Identify the blood parasite species.
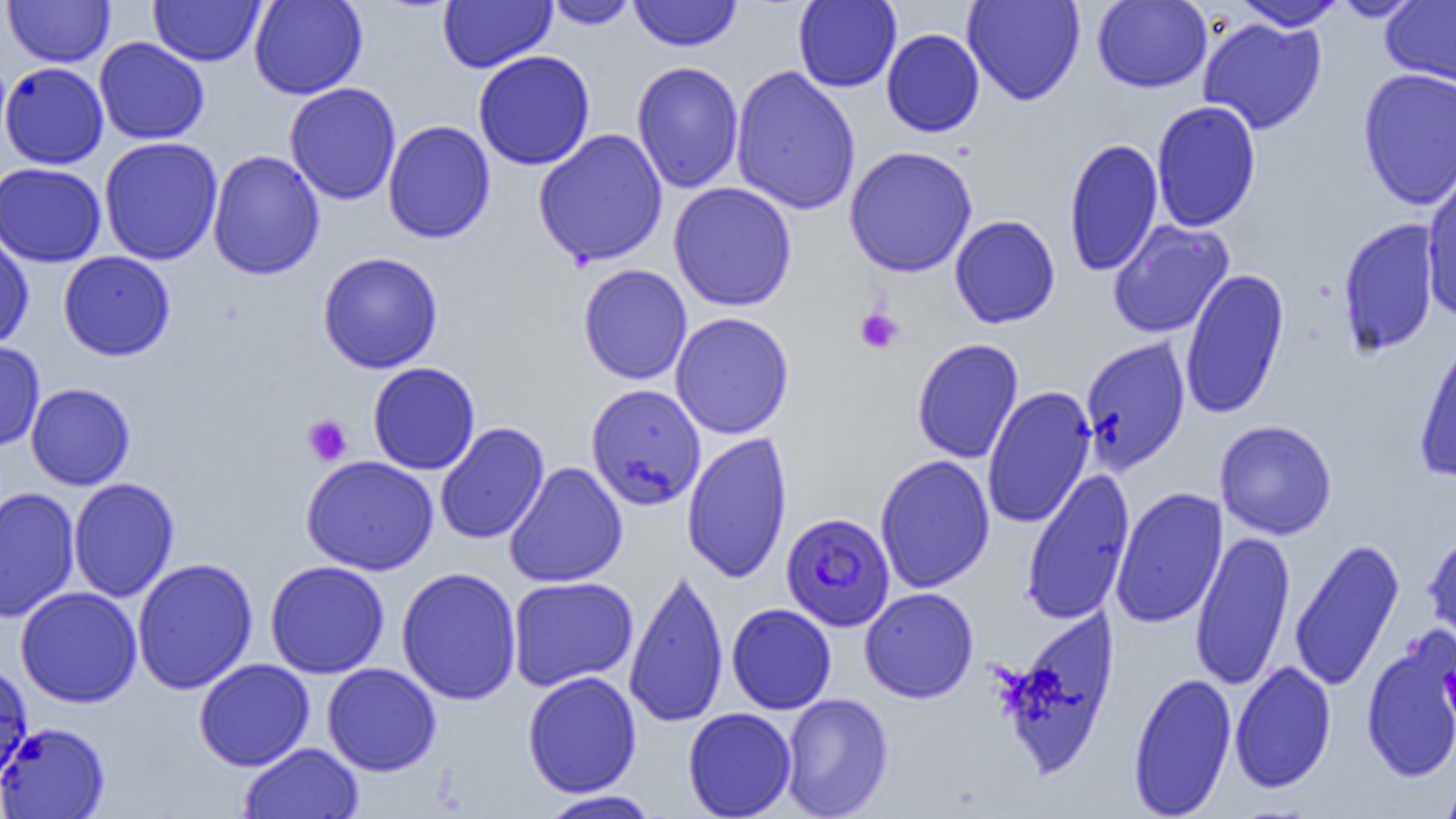

Plasmodium falciparum.

field of view = one of a larger specimen
preparation = thin blood film
image size = 1456×819 pixels
magnification = 1000x
modality = light microscopy
Plasmodium falciparum-infected red blood cell locations = approximate bounding boxes as (x1,y1)-(x2,y2) corner pairs in pixels: (781,512)-(895,631)
platelet locations = approximate bounding boxes as (x1,y1)-(x2,y2) corner pairs in pixels: (855,307)-(904,355), (302,414)-(353,466)
uninfected red blood cell locations = approximate bounding boxes as (x1,y1)-(x2,y2) corner pairs in pixels: (149,0)-(264,66), (249,0)-(367,99), (438,0)-(556,73), (544,0)-(639,29), (793,0)-(902,92), (962,0)-(1086,106), (1092,0)-(1212,93), (1331,0)-(1426,21), (3,1)-(115,67), (628,1)-(742,51), (1232,1)-(1347,31), (1381,1)-(1456,87), (1197,17)-(1327,135), (881,28)-(985,138), (94,37)-(210,144), (473,50)-(596,171), (631,61)-(744,193), (0,62)-(109,169), (731,65)-(861,216), (1357,68)-(1456,210), (284,83)-(401,205), (1151,100)-(1261,231), (383,120)-(496,244), (533,128)-(668,267), (99,136)-(223,265), (1064,137)-(1164,277), (844,146)-(978,277), (207,150)-(324,280), (0,162)-(106,266), (1421,166)-(1456,322), (668,182)-(797,311), (950,214)-(1061,329), (1337,218)-(1442,357), (1107,220)-(1234,338), (0,233)-(34,351), (58,251)-(175,361), (317,251)-(444,373), (578,263)-(692,384), (1179,268)-(1290,419), (670,312)-(794,439), (1413,329)-(1456,483), (1079,337)-(1190,474), (912,338)-(1024,464), (0,341)-(45,452), (367,362)-(480,474), (26,383)-(135,490), (586,384)-(706,511), (981,386)-(1096,529), (1215,420)-(1337,540), (434,422)-(550,544), (681,432)-(793,584), (875,454)-(994,594), (301,455)-(439,576), (504,461)-(628,588), (1020,468)-(1135,625), (67,477)-(180,602), (1111,486)-(1227,629), (0,487)-(80,621), (1190,530)-(1295,692), (1423,530)-(1456,652), (1289,537)-(1405,693), (132,557)-(258,694), (265,560)-(390,678), (624,565)-(729,729), (396,566)-(522,705), (507,576)-(638,691), (15,586)-(142,708), (860,587)-(978,703), (726,603)-(836,715), (998,608)-(1120,780), (1361,630)-(1456,784), (194,658)-(314,771), (0,661)-(33,786), (1229,661)-(1336,793), (322,663)-(441,776), (522,671)-(642,797), (1127,671)-(1237,818), (781,693)-(893,818), (683,708)-(797,818), (0,722)-(110,819), (239,742)-(363,819), (1439,769)-(1456,819), (538,790)-(662,818)